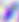

modality = micrograph
identification = Toxoplasma gondii
magnification = 400x